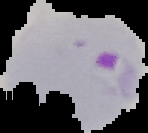
result = malaria parasites detected
preparation = thin blood smear
image size = 148×133 pixels
image type = segmented cell region with the area outside set to black